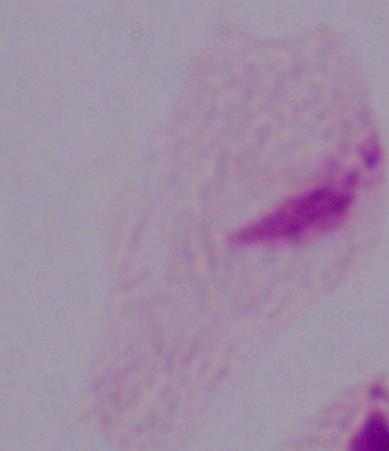

Summary:
  - Modality: micrograph
  - Magnification: 1000x
  - Identification: trichomonad